Classify this cell by malaria status.
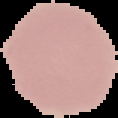

Uninfected.

From a thin blood film. Segmented cell region on a black background. Image is 118×118 pixels.